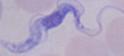

Summary:
  - Magnification: 1000x
  - Modality: micrograph
  - Identification: trypanosome